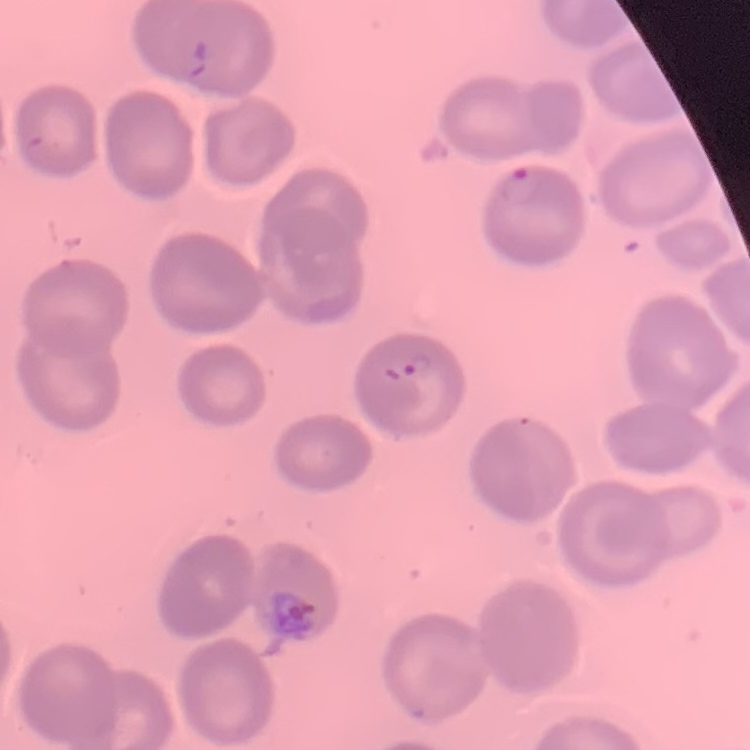
{
  "red_blood_cell_morphology": "no rouleaux formation",
  "image_type": "square crop of a larger photomicrograph",
  "preparation": "thin peripheral smear",
  "stain": "Field's or Giemsa"
}